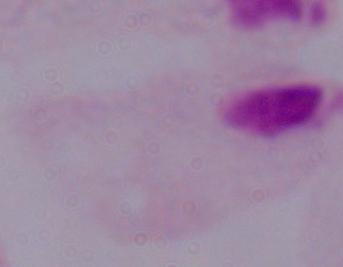
modality = micrograph
magnification = 1000x
identification = trichomonad